Name the parasite shown.
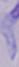

This is a trypanosome.

Summary:
  - Modality: micrograph
  - Magnification: 1000x